Identify the blood parasite species.
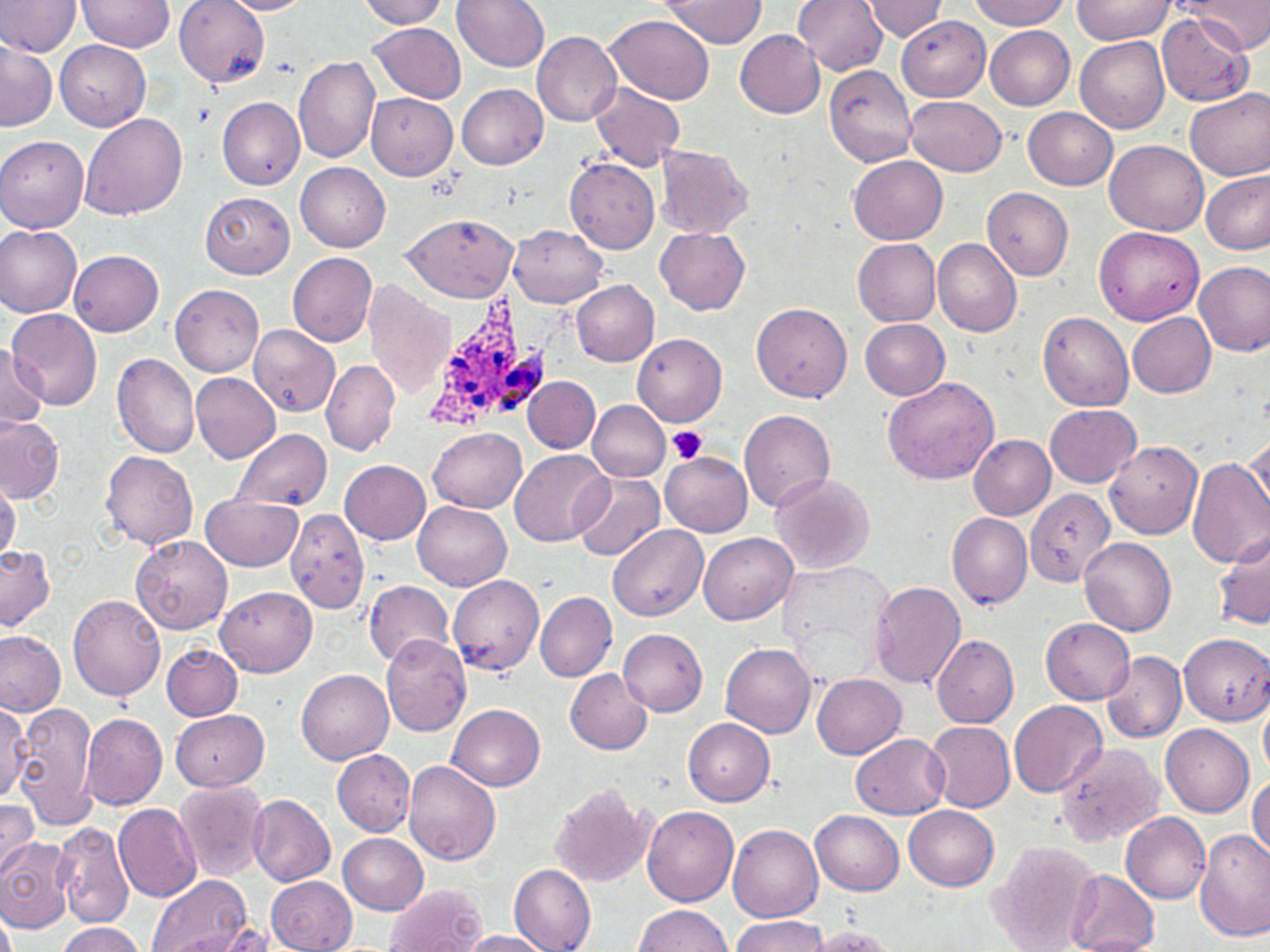
Plasmodium ovale.

Summary:
  - Coordinate format: approximate bounding boxes as (x1,y1)-(x2,y2) corner pairs in pixels
  - Uninfected red blood cell locations: (1,0)-(80,57), (78,0)-(174,53), (175,0)-(270,87), (218,0)-(314,16), (357,0)-(451,28), (455,0)-(550,71), (792,0)-(888,75), (861,0)-(947,40), (969,0)-(1072,28), (1184,0)-(1269,54), (660,1)-(767,47), (1072,1)-(1173,44), (1157,12)-(1253,106), (604,13)-(716,103), (898,15)-(988,101), (370,21)-(468,102), (986,27)-(1074,109), (735,29)-(825,118), (531,31)-(622,125), (1075,36)-(1170,131), (0,39)-(55,132), (56,40)-(151,131), (294,55)-(381,163), (824,65)-(917,168), (590,81)-(686,170), (456,84)-(547,169), (1185,87)-(1270,182), (366,93)-(458,180), (216,96)-(304,190), (906,96)-(1006,174), (1023,107)-(1117,190), (78,112)-(187,219), (0,135)-(89,233), (1105,141)-(1208,235), (654,144)-(753,238), (850,156)-(948,244), (564,157)-(659,254), (297,164)-(390,251), (1201,170)-(1269,255), (981,187)-(1072,279), (199,190)-(294,278), (400,213)-(520,302), (509,224)-(607,307), (0,225)-(82,318), (656,226)-(751,314), (1094,226)-(1205,326), (852,237)-(941,326), (932,238)-(1022,338), (70,250)-(164,336), (287,252)-(377,345), (1194,261)-(1270,356), (572,281)-(660,366), (364,282)-(454,397), (171,284)-(262,376), (752,303)-(852,403), (9,307)-(103,410), (1038,310)-(1132,412), (1128,313)-(1216,398), (860,319)-(950,400), (250,324)-(339,417), (633,333)-(728,427), (0,342)-(48,432), (111,353)-(199,458), (321,358)-(400,455), (190,371)-(281,463), (524,377)-(601,452), (882,377)-(999,484), (587,400)-(669,481), (1045,403)-(1141,486), (740,409)-(835,513), (0,415)-(65,503), (231,428)-(331,513), (427,428)-(526,512), (1245,433)-(1270,515), (968,434)-(1056,520), (1105,439)-(1202,538), (509,449)-(608,546), (101,451)-(198,550), (659,452)-(752,536), (1186,455)-(1270,569), (341,459)-(431,545), (571,471)-(664,562), (768,473)-(876,574), (0,477)-(20,561), (1024,487)-(1116,589), (202,495)-(300,570), (414,500)-(512,591), (290,508)-(371,615), (947,513)-(1034,610), (607,524)-(708,623), (1214,528)-(1270,632), (699,532)-(798,625), (132,534)-(232,634), (1080,539)-(1176,636), (0,544)-(54,632), (448,575)-(545,676), (364,580)-(453,668), (869,581)-(966,690), (215,585)-(316,677), (535,592)-(616,682), (68,593)-(166,700), (1040,618)-(1134,703), (618,629)-(707,716), (0,630)-(67,717), (1178,632)-(1270,725), (930,633)-(1017,728), (380,634)-(472,738), (720,642)-(816,738), (161,643)-(243,719), (1101,651)-(1187,742), (564,668)-(652,754), (297,669)-(394,764), (812,673)-(906,759), (0,697)-(29,802), (1260,697)-(1270,779), (1009,699)-(1106,799), (10,702)-(99,830), (449,703)-(546,790), (169,707)-(269,791), (81,713)-(166,810), (684,718)-(775,805), (925,721)-(1015,812), (1160,724)-(1254,817), (851,732)-(950,818), (1052,740)-(1165,848), (332,749)-(416,836), (402,761)-(500,867), (1247,774)-(1269,861), (174,780)-(269,882), (547,781)-(657,888), (248,794)-(337,886), (0,802)-(38,876), (112,803)-(202,902), (642,804)-(738,907), (903,805)-(999,890), (811,810)-(903,895), (1120,811)-(1210,903), (54,822)-(136,928), (728,824)-(822,922), (1195,830)-(1270,942), (339,833)-(428,914), (0,837)-(74,934), (990,843)-(1100,950), (509,865)-(596,951), (1063,869)-(1160,952), (148,874)-(253,952), (267,875)-(357,952), (386,884)-(485,952), (633,904)-(733,952), (730,916)-(828,952), (54,922)-(145,952), (802,924)-(898,951), (158,929)-(266,952), (452,930)-(557,951)
  - Platelet locations: (191,103)-(213,127), (667,425)-(709,467)
  - Plasmodium ovale-infected red blood cell locations: (424,290)-(575,437)
  - Modality: light microscopy
  - Magnification: 1000x
  - Stain: May-Grünwald-Giemsa
  - Preparation: thin blood film
  - Image size: 1270×952 pixels
  - Field of view: single